Name the cell type shown.
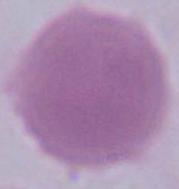

An erythrocyte.

Summary:
  - Magnification: 1000x
  - Modality: photomicrograph